Name the parasite shown.
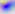
This is Toxoplasma gondii.

Summary:
  - Magnification: 400x
  - Modality: micrograph